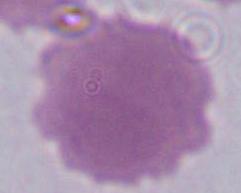

magnification: 1000x
identification: erythrocyte
modality: photomicrograph